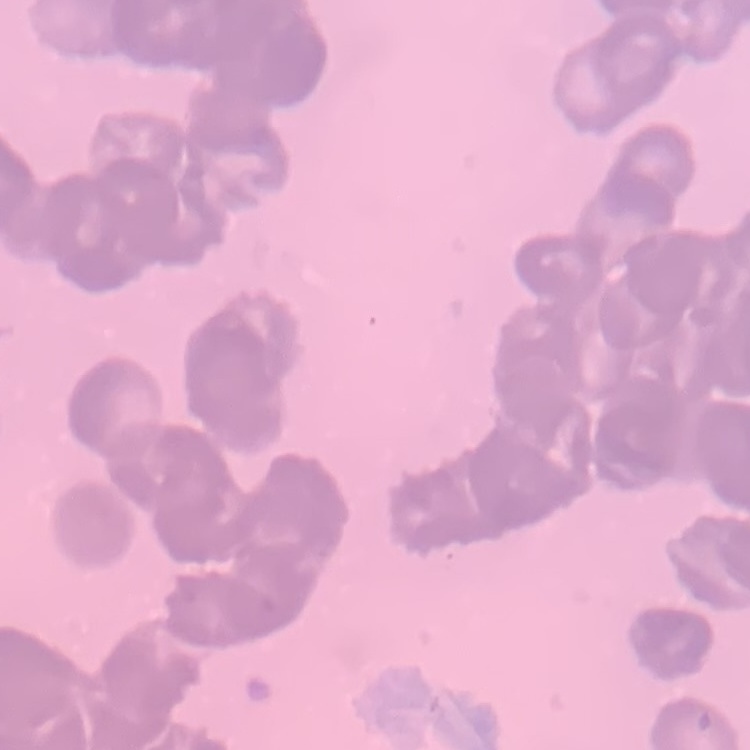

{
  "erythrocyte_morphology": "rouleaux formation",
  "preparation": "thin blood smear",
  "image_type": "one tile cut from a larger photomicrograph",
  "stain": "Field's or Giemsa"
}